Locate platelets.
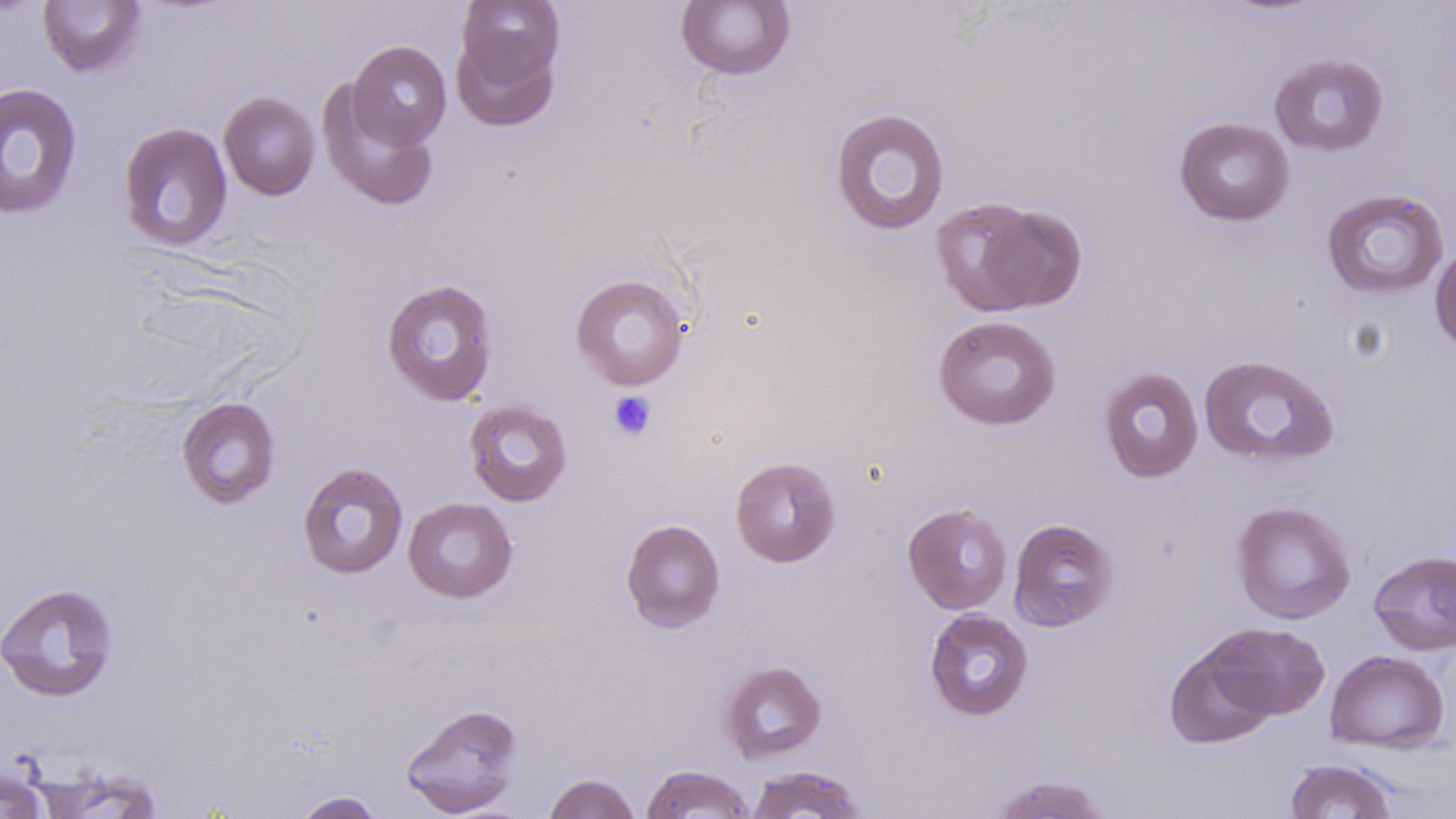
Approximate bounding boxes as named x1/y1/x2/y2 corners in pixels.
Platelets: (x1=608, y1=391, x2=656, y2=441).

slide-level diagnosis = no evidence of blood parasites
modality = light microscopy
preparation = thin blood film
uninfected red blood cell locations = approximate bounding boxes as named x1/y1/x2/y2 corners in pixels: (x1=37, y1=0, x2=147, y2=77), (x1=456, y1=1, x2=566, y2=90), (x1=675, y1=1, x2=796, y2=80), (x1=452, y1=33, x2=561, y2=132), (x1=347, y1=40, x2=451, y2=149), (x1=1268, y1=52, x2=1389, y2=157), (x1=316, y1=81, x2=439, y2=212), (x1=0, y1=83, x2=83, y2=218), (x1=218, y1=91, x2=320, y2=201), (x1=829, y1=106, x2=951, y2=237), (x1=1174, y1=116, x2=1295, y2=226), (x1=118, y1=122, x2=233, y2=252), (x1=1321, y1=188, x2=1450, y2=300), (x1=930, y1=196, x2=1081, y2=317), (x1=1430, y1=242, x2=1456, y2=354), (x1=570, y1=273, x2=689, y2=390), (x1=381, y1=278, x2=499, y2=407), (x1=932, y1=314, x2=1062, y2=430), (x1=1198, y1=354, x2=1341, y2=468), (x1=1098, y1=365, x2=1205, y2=483), (x1=176, y1=396, x2=281, y2=509), (x1=463, y1=399, x2=573, y2=507), (x1=729, y1=455, x2=841, y2=567), (x1=296, y1=461, x2=409, y2=579), (x1=403, y1=497, x2=518, y2=604), (x1=1231, y1=500, x2=1356, y2=624), (x1=903, y1=503, x2=1013, y2=614), (x1=1008, y1=517, x2=1119, y2=632), (x1=621, y1=518, x2=725, y2=633), (x1=1368, y1=549, x2=1456, y2=655), (x1=0, y1=582, x2=121, y2=702), (x1=924, y1=608, x2=1034, y2=721), (x1=1204, y1=621, x2=1330, y2=721), (x1=1164, y1=644, x2=1278, y2=750), (x1=1325, y1=649, x2=1450, y2=754), (x1=717, y1=659, x2=827, y2=764), (x1=400, y1=702, x2=524, y2=817), (x1=1284, y1=758, x2=1399, y2=818), (x1=639, y1=764, x2=756, y2=818), (x1=745, y1=764, x2=869, y2=818), (x1=0, y1=765, x2=52, y2=819), (x1=542, y1=772, x2=641, y2=819), (x1=987, y1=773, x2=1110, y2=818), (x1=290, y1=790, x2=386, y2=819)
stain = May-Grünwald-Giemsa
image size = 1456×819 pixels
magnification = 1000x
field of view = single